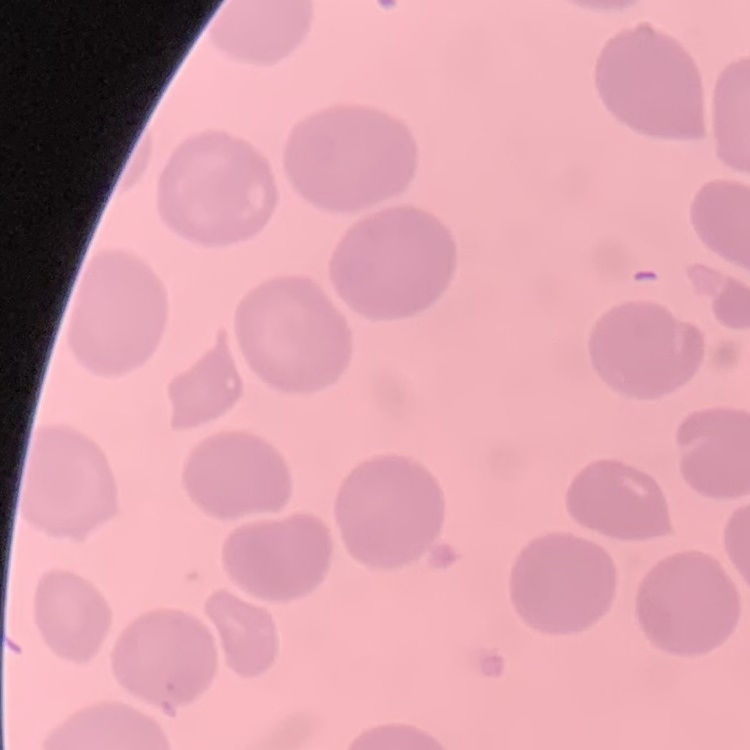
{
  "erythrocyte_morphology": "no rouleaux formation",
  "preparation": "thin blood smear",
  "stain": "Field's or Giemsa",
  "image_type": "square crop of a larger photomicrograph"
}